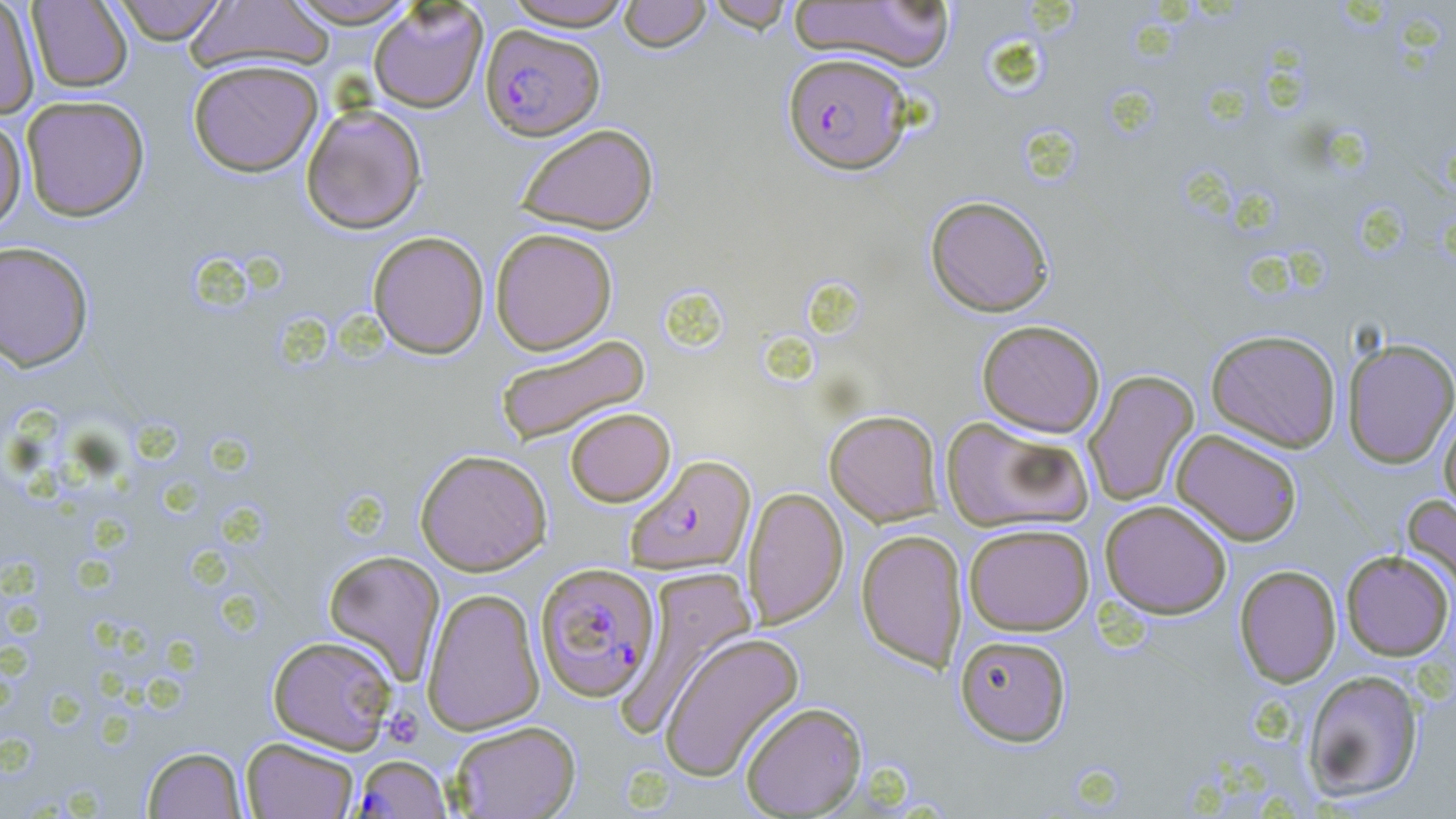

Approximate bounding boxes as [x1, y1, x2, y2] in pixels. Plasmodium falciparum-infected red blood cell locations: [480, 24, 605, 140], [783, 52, 913, 174], [626, 454, 755, 574], [534, 563, 660, 702], [352, 754, 452, 818]. Uninfected red blood cell locations: [0, 0, 40, 120], [108, 0, 229, 44], [280, 0, 422, 28], [502, 0, 636, 30], [704, 0, 796, 32], [26, 1, 133, 93], [187, 1, 337, 75], [618, 1, 711, 52], [788, 1, 958, 71], [368, 2, 488, 113], [187, 58, 323, 177], [21, 94, 150, 221], [300, 103, 428, 234], [0, 115, 27, 236], [515, 123, 659, 235], [925, 194, 1054, 317], [490, 228, 618, 355], [367, 230, 490, 359], [0, 240, 94, 372], [976, 319, 1105, 438], [1205, 329, 1341, 452], [494, 334, 652, 447], [1342, 337, 1456, 469], [1083, 370, 1199, 507], [1438, 404, 1456, 521], [565, 407, 675, 507], [824, 410, 943, 526], [941, 416, 1095, 533], [1171, 429, 1303, 546], [414, 448, 552, 576], [743, 486, 848, 629], [1401, 493, 1456, 604], [1100, 499, 1232, 619], [964, 523, 1095, 636], [856, 529, 967, 672], [323, 549, 446, 683], [1341, 550, 1454, 660], [1234, 565, 1341, 687], [616, 566, 759, 734], [421, 587, 545, 735], [658, 631, 805, 782], [954, 634, 1072, 747], [267, 635, 399, 753], [1302, 668, 1425, 803], [740, 701, 867, 817], [449, 720, 581, 818], [240, 737, 359, 818], [142, 746, 247, 818]. Platelet locations: [382, 706, 423, 748]. Slide-level diagnosis: Plasmodium falciparum. Thin blood film. May-Grünwald-Giemsa stain. Captured at 1000x magnification. Light microscopy. Image is 1456×819 pixels. Single field of view.